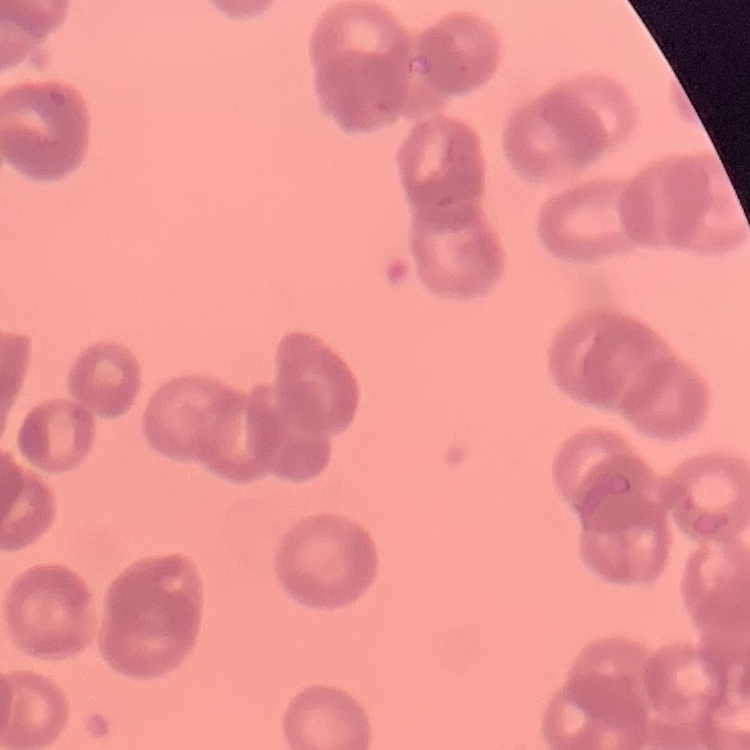

Summary:
  - Erythrocyte morphology: rouleaux formation
  - Stain: Field's or Giemsa
  - Preparation: thin blood smear
  - Image type: square crop of a larger photomicrograph